Comment on the morphology of the red blood cells.
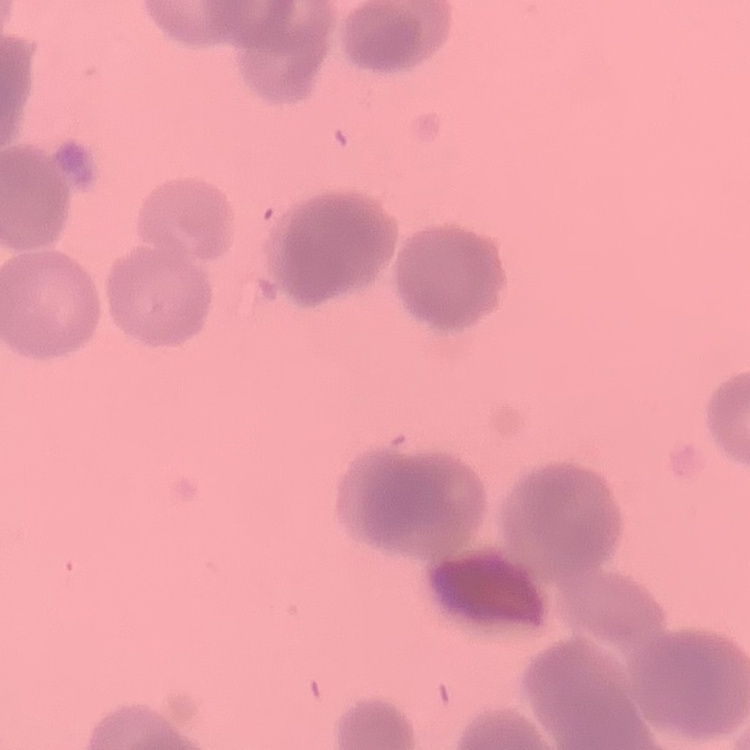
They show rouleaux formation.

Summary:
  - Stain: Field's or Giemsa
  - Preparation: thin blood film
  - Image type: one tile cut from a larger photomicrograph